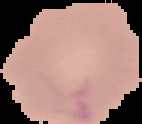
Malaria status: uninfected. Image is 142×124 pixels. Segmented cell region on a black background. From a thin blood film.